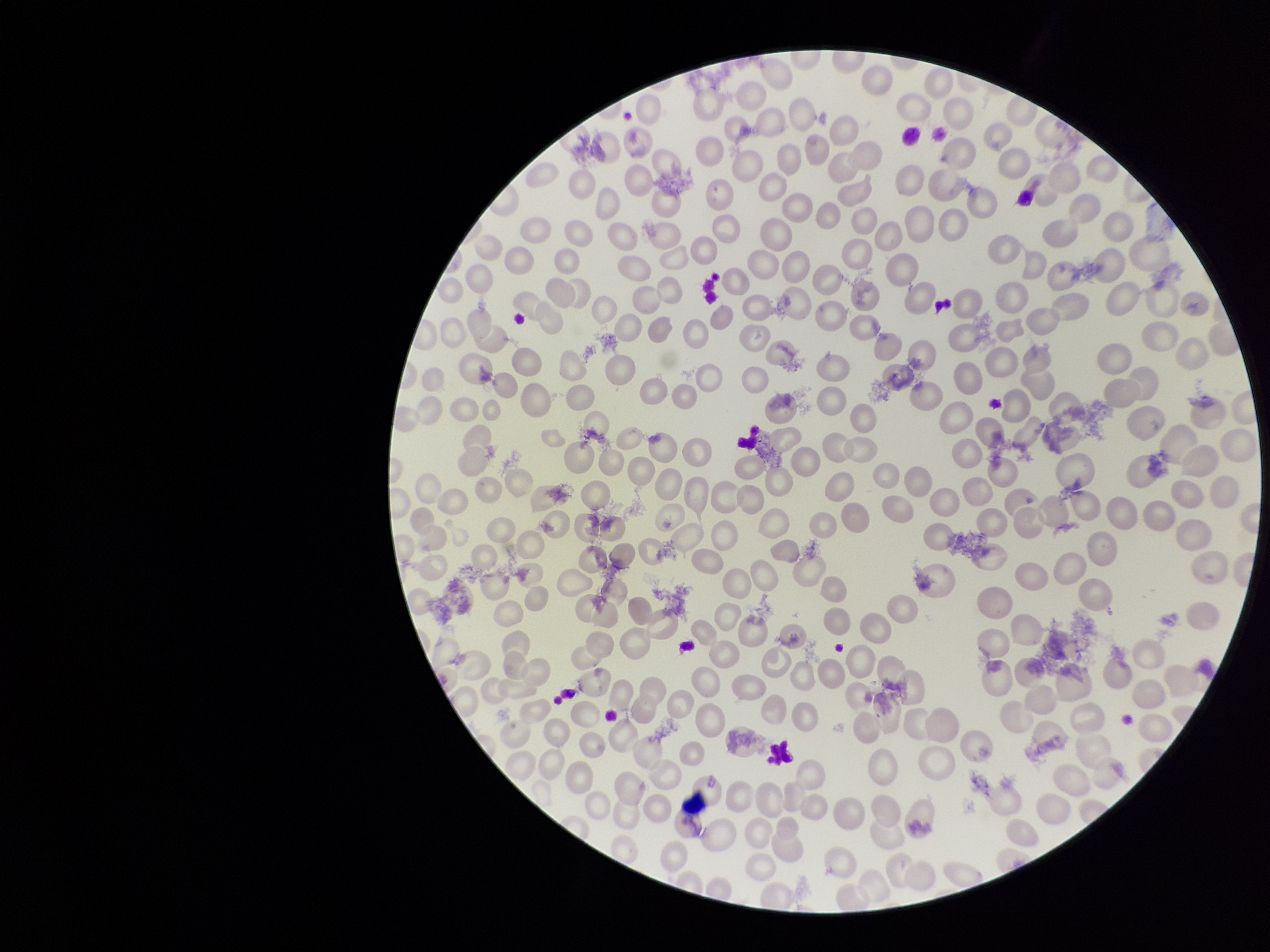

Image is 1270×952 pixels. Stained with Giemsa. Parasitized red blood cells: none seen. Red blood cell count: 249. Parasitized red blood cell count: 0. Smartphone photograph taken through the eyepiece of a microscope. Preparation: thin blood smear. Single field of view. Patient malaria status: negative.